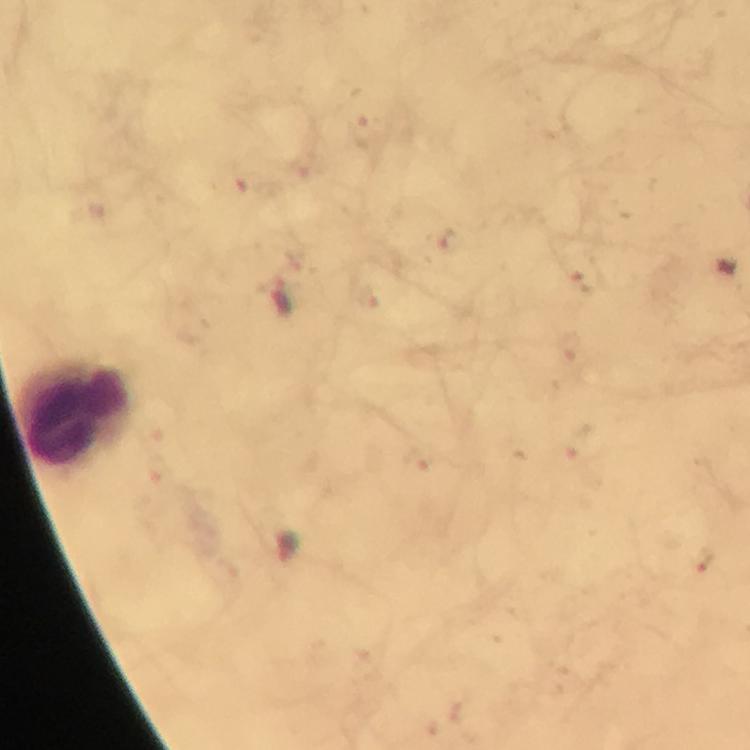
context: from a diagnostic examination for malaria
leukocyte_locations: 'approximate centers as {x, y} in pixels: {74, 412}'
capture: smartphone mounted on the microscope
plasmodium_parasite_locations: 'approximate centers as {x, y} in pixels: {449, 242}, {584, 274}, {282, 295}, {288, 546}, {704, 559}'
stain: Giemsa
image_size: 750×750 pixels
immersion_oil: used
magnification: 100x
preparation: thick blood film
cropped_from: one field of view